Identify the blood parasite species.
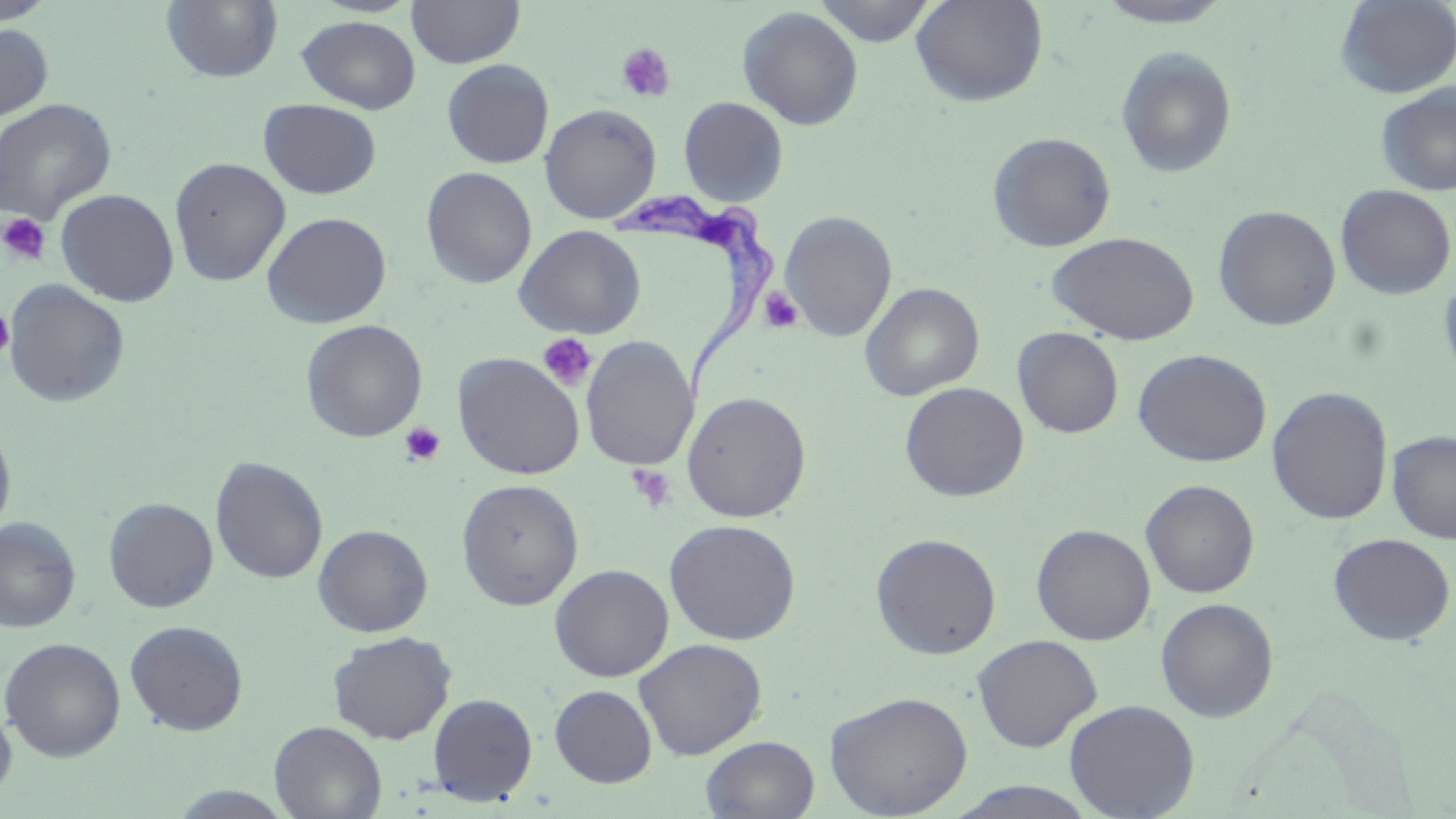

Trypanosoma brucei.

Summary:
  - Coordinate format: approximate bounding boxes as named x1/y1/x2/y2 corners in pixels
  - Platelet locations: (x1=616, y1=42, x2=676, y2=103), (x1=0, y1=213, x2=51, y2=266), (x1=759, y1=287, x2=803, y2=335), (x1=0, y1=306, x2=15, y2=362), (x1=537, y1=333, x2=597, y2=391), (x1=399, y1=422, x2=446, y2=466), (x1=628, y1=464, x2=676, y2=513)
  - Uninfected red blood cell locations: (x1=0, y1=0, x2=57, y2=24), (x1=160, y1=0, x2=283, y2=83), (x1=407, y1=0, x2=525, y2=68), (x1=813, y1=0, x2=937, y2=46), (x1=911, y1=0, x2=1048, y2=107), (x1=1094, y1=0, x2=1236, y2=28), (x1=1335, y1=0, x2=1456, y2=98), (x1=737, y1=6, x2=864, y2=130), (x1=296, y1=15, x2=421, y2=114), (x1=0, y1=23, x2=53, y2=122), (x1=1116, y1=46, x2=1238, y2=180), (x1=442, y1=59, x2=554, y2=168), (x1=1375, y1=83, x2=1456, y2=196), (x1=678, y1=96, x2=788, y2=206), (x1=0, y1=98, x2=117, y2=225), (x1=258, y1=99, x2=382, y2=199), (x1=540, y1=103, x2=661, y2=224), (x1=987, y1=132, x2=1116, y2=252), (x1=169, y1=157, x2=291, y2=287), (x1=421, y1=167, x2=537, y2=289), (x1=1336, y1=184, x2=1456, y2=300), (x1=55, y1=189, x2=179, y2=306), (x1=1213, y1=205, x2=1342, y2=331), (x1=780, y1=210, x2=898, y2=342), (x1=262, y1=212, x2=392, y2=328), (x1=514, y1=225, x2=646, y2=338), (x1=1047, y1=231, x2=1200, y2=345), (x1=1439, y1=273, x2=1456, y2=390), (x1=3, y1=280, x2=130, y2=408), (x1=861, y1=282, x2=985, y2=401), (x1=300, y1=319, x2=427, y2=443), (x1=1013, y1=327, x2=1124, y2=438), (x1=580, y1=336, x2=699, y2=472), (x1=1133, y1=348, x2=1271, y2=467), (x1=452, y1=352, x2=585, y2=480), (x1=899, y1=381, x2=1029, y2=502), (x1=1267, y1=386, x2=1393, y2=525), (x1=681, y1=391, x2=812, y2=523), (x1=0, y1=421, x2=17, y2=542), (x1=1387, y1=431, x2=1456, y2=543), (x1=210, y1=456, x2=328, y2=584), (x1=456, y1=478, x2=584, y2=611), (x1=1140, y1=479, x2=1260, y2=598), (x1=103, y1=497, x2=219, y2=613), (x1=0, y1=518, x2=81, y2=633), (x1=664, y1=518, x2=801, y2=645), (x1=1031, y1=523, x2=1156, y2=645), (x1=313, y1=524, x2=434, y2=637), (x1=1328, y1=532, x2=1455, y2=646), (x1=870, y1=533, x2=1002, y2=659), (x1=550, y1=563, x2=674, y2=682), (x1=1155, y1=597, x2=1279, y2=722), (x1=125, y1=620, x2=248, y2=736), (x1=328, y1=631, x2=456, y2=745), (x1=972, y1=634, x2=1102, y2=752), (x1=0, y1=637, x2=125, y2=762), (x1=633, y1=638, x2=767, y2=760), (x1=549, y1=685, x2=657, y2=787), (x1=825, y1=690, x2=973, y2=818), (x1=427, y1=693, x2=538, y2=805), (x1=1063, y1=698, x2=1200, y2=819), (x1=0, y1=699, x2=17, y2=806), (x1=269, y1=720, x2=387, y2=819), (x1=700, y1=735, x2=820, y2=818), (x1=945, y1=781, x2=1102, y2=819), (x1=161, y1=784, x2=299, y2=817)
  - Trypanosoma brucei locations: (x1=611, y1=189, x2=781, y2=402)
  - Image size: 1456×819 pixels
  - Field of view: one of a larger specimen
  - Modality: optical microscopy
  - Preparation: thin blood smear
  - Magnification: 1000x
  - Stain: May-Grünwald-Giemsa